Give the position of every Plasmodium parasite visible.
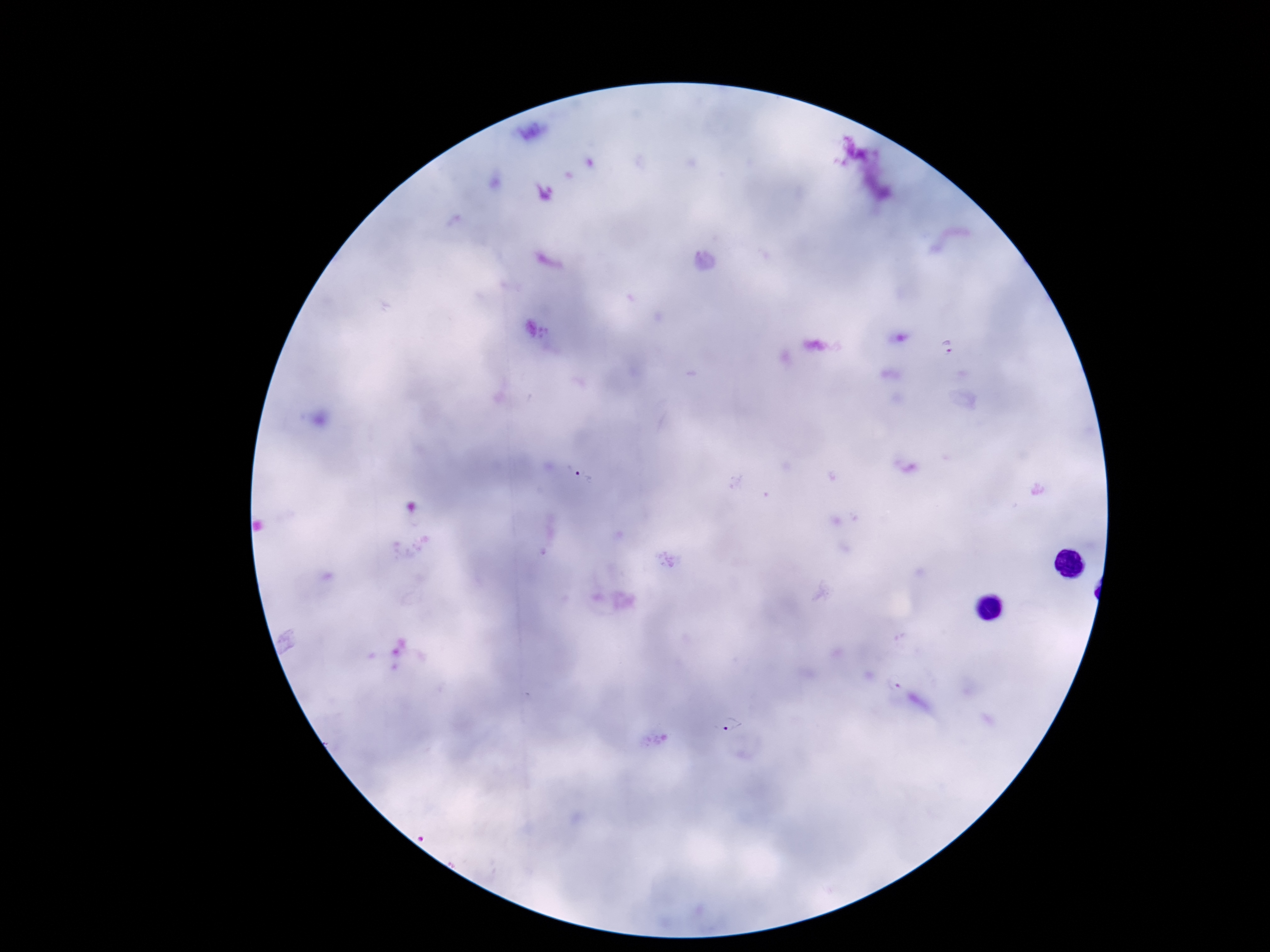

Approximate centers as {x, y} in pixels.
Plasmodium parasites: {945, 346}, {585, 476}, {733, 726}.

{
  "capture": "smartphone camera through the microscope eyepiece",
  "stain": "Giemsa",
  "preparation": "thick blood film",
  "magnification": "100x",
  "field_of_view": "single",
  "image_size": "1270×952 pixels",
  "patient_malaria_status": "infected"
}